State which parasite is depicted.
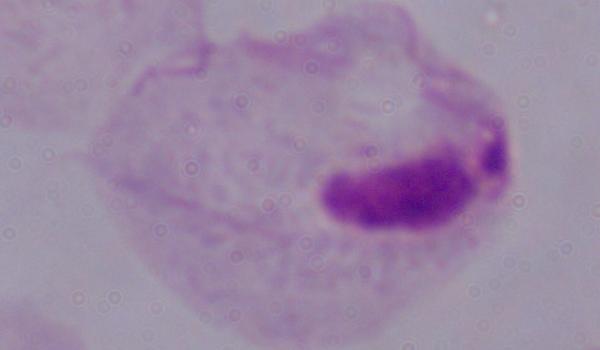

A trichomonad.

Captured at 1000x magnification. Micrograph.